Comment on the morphology of the erythrocytes.
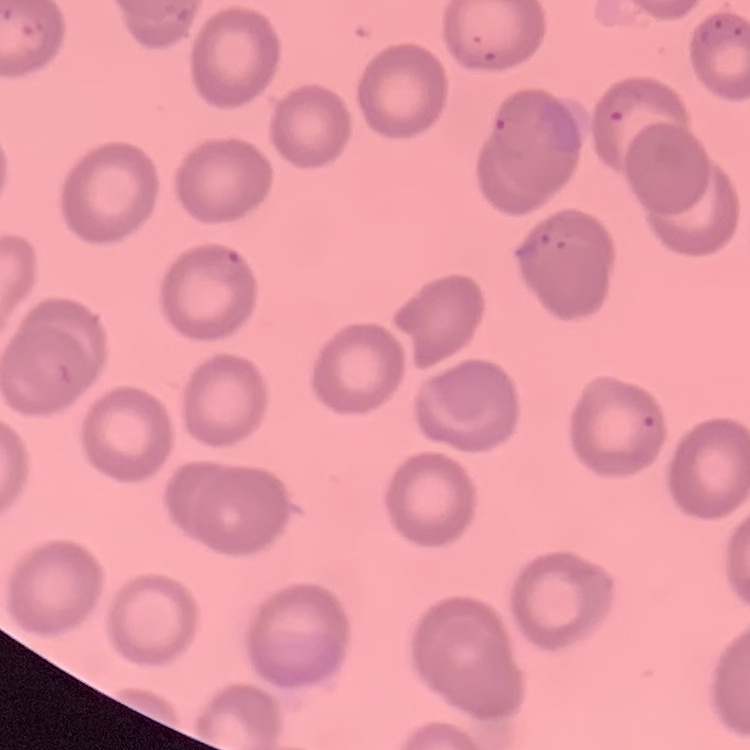

They show no rouleaux formation.

Stained with either Field's or Giemsa. Square crop of a larger photomicrograph. Thin blood smear.